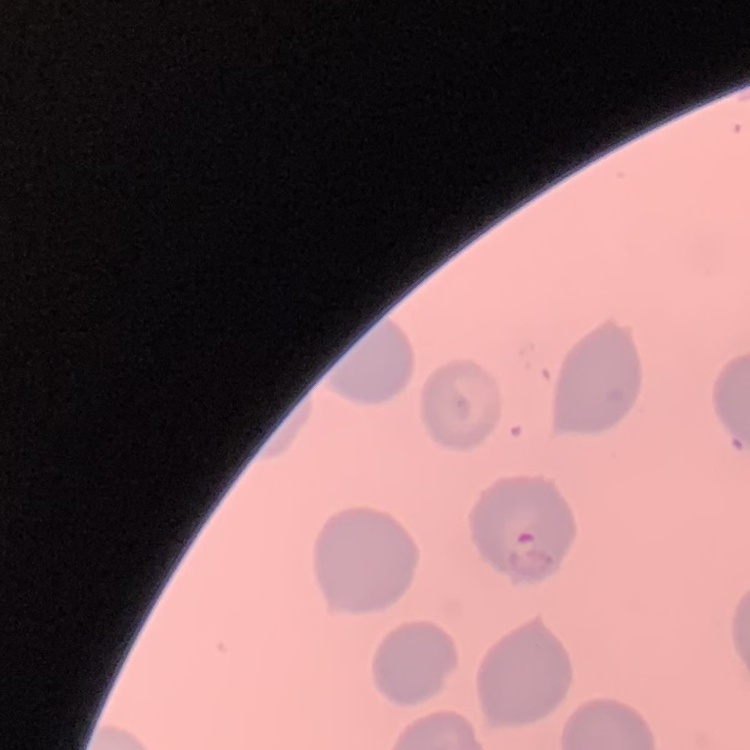
Summary:
  - Red blood cell morphology: no rouleaux formation
  - Image type: square crop of a larger photomicrograph
  - Stain: Field's or Giemsa
  - Preparation: thin blood film